Classify this cell by malaria status.
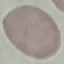
Uninfected.

image type = cell patch, automatically extracted from a larger field of view and resized to 64 × 64 pixels
preparation = thin blood film
stain = Giemsa
capture = smartphone camera at the microscope eyepiece